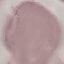
result = negative for malaria parasites
preparation = thin blood smear
stain = Giemsa
capture = smartphone camera at the microscope eyepiece
image type = automatically extracted cell patch, resized to 64 × 64 pixels